Report the malaria status of this cell.
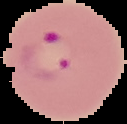
It is parasitized.

Summary:
  - Image size: 127×124 pixels
  - Image type: segmented cell region on a black background
  - Preparation: thin blood film